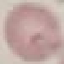

malaria status = uninfected
image type = automatically extracted cell patch, resized to 64 × 64 pixels
preparation = thin smear
capture = smartphone camera at the microscope eyepiece
stain = Giemsa